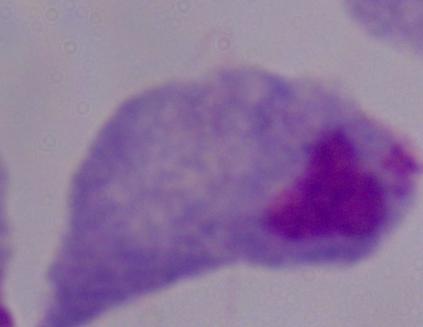
magnification = 1000x
identification = trichomonad
modality = micrograph